Classify this cell by malaria status.
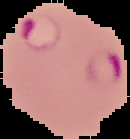
It is parasitized.

image_size: 130×139 pixels
image_type: cell region segmented out of the field of view; surrounding area masked to black
preparation: thin blood smear